Name the parasite shown.
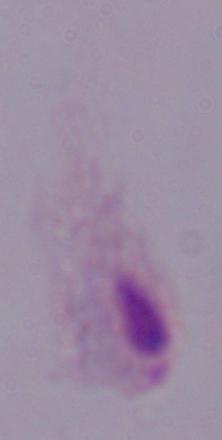
This is a trichomonad.

1000x magnification. Photomicrograph.